Classify this cell by malaria status.
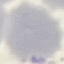
It is uninfected.

Thin blood film. Automatically extracted cell patch, resized to 64 × 64 pixels. Photographed with a smartphone camera at the microscope eyepiece. Giemsa-stained preparation.